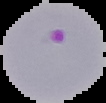

Summary:
  - Preparation: thin blood film
  - Image size: 106×103 pixels
  - Result: Plasmodium parasites identified
  - Image type: segmented cell region with the area outside set to black